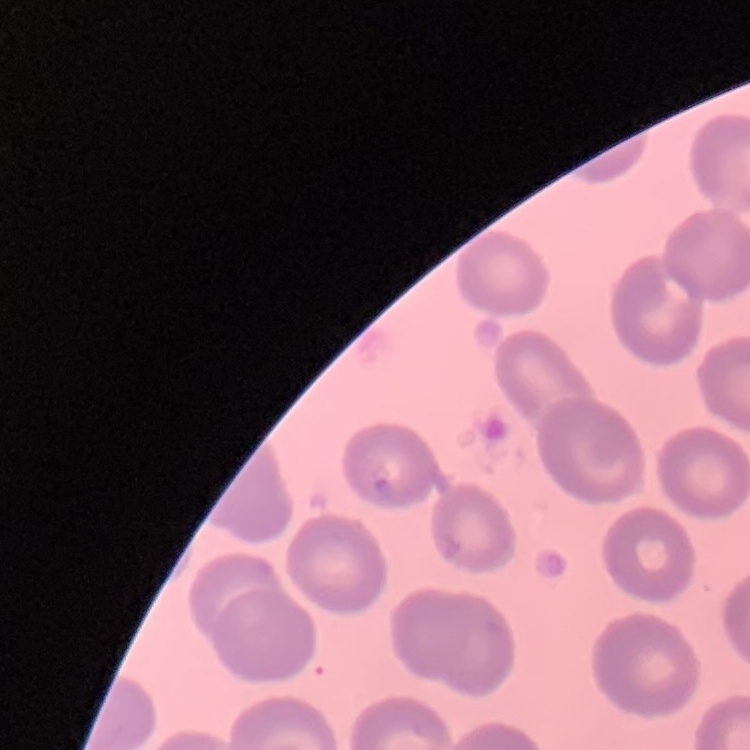

red blood cell morphology = no rouleaux formation
image type = square crop of a larger photomicrograph
stain = Field's or Giemsa
preparation = thin blood smear